Comment on the morphology of the red blood cells.
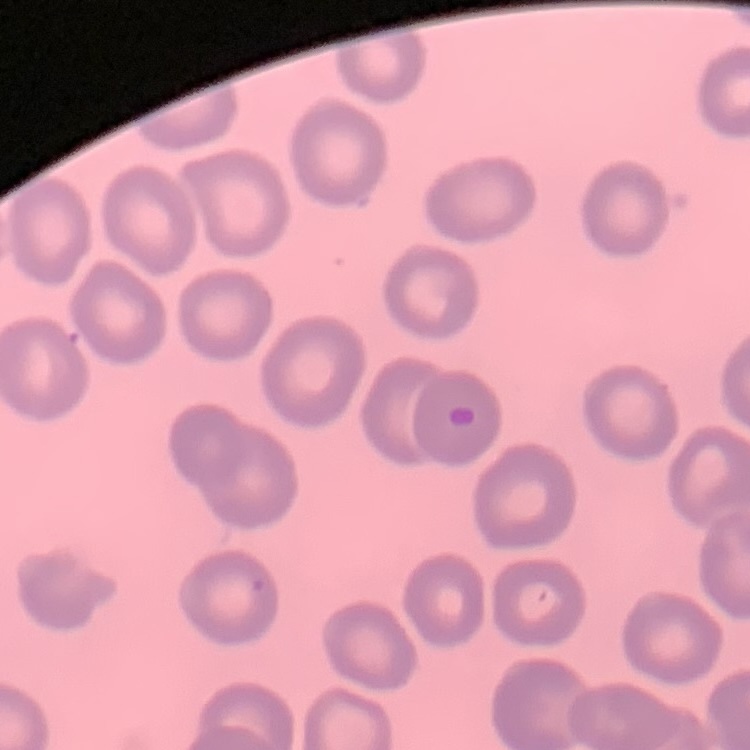
No rouleaux formation.

Summary:
  - Preparation: thin blood smear
  - Stain: Field's or Giemsa
  - Image type: one tile cut from a larger photomicrograph